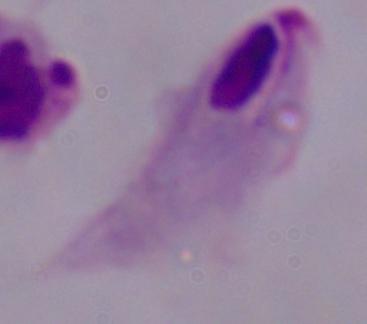

modality = micrograph
magnification = 1000x
identification = trichomonad